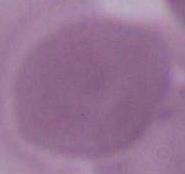

Photomicrograph. An erythrocyte is shown. Captured at 1000x magnification.